Locate and identify every blood parasite.
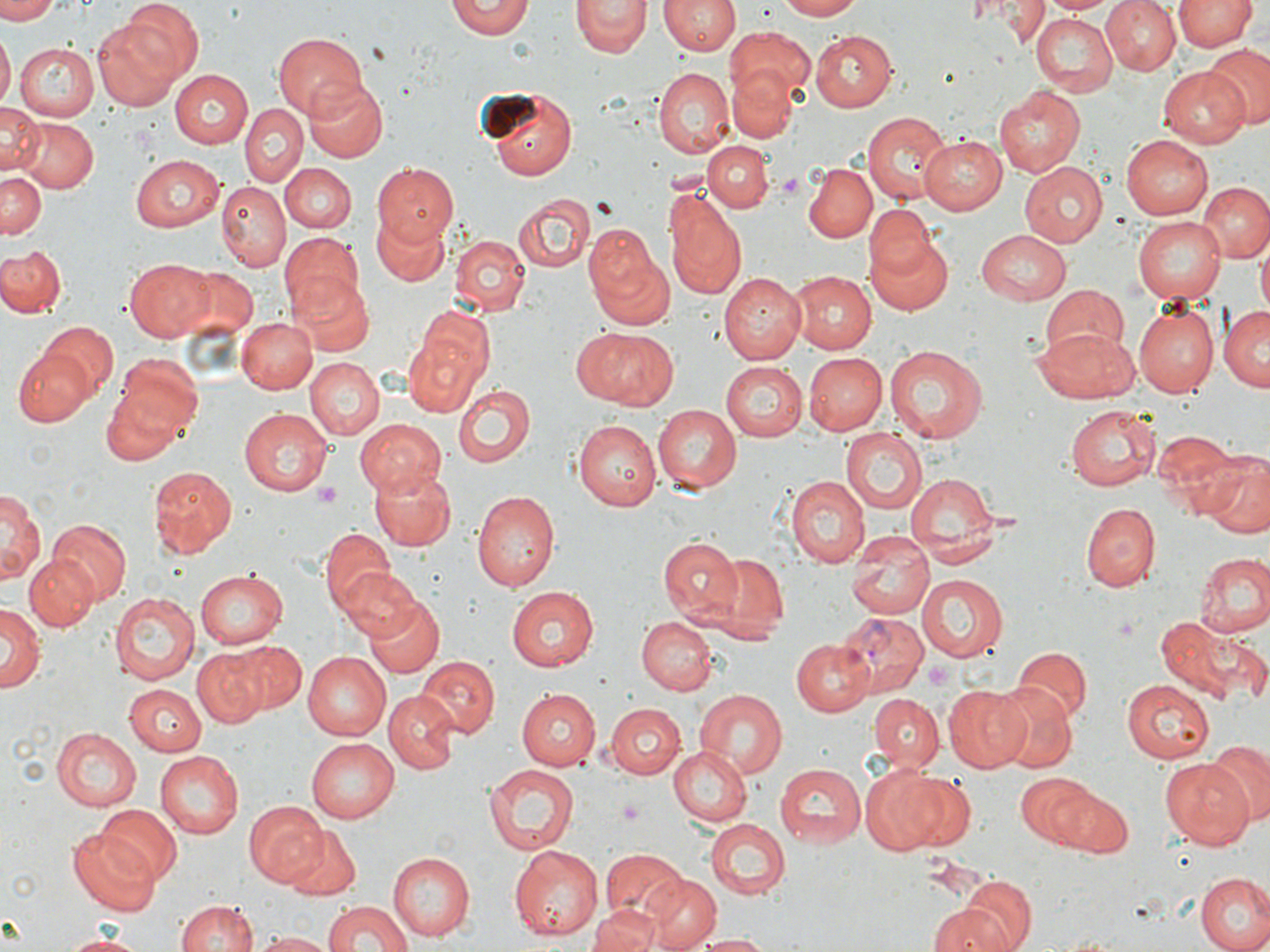
Approximate bounding boxes as named x1/y1/x2/y2 corners in pixels.
Plasmodium vivax-infected red blood cells: (x1=834, y1=614, x2=934, y2=701).
No Plasmodium falciparum, Plasmodium ovale, Plasmodium malariae, Babesia divergens, or Trypanosoma brucei observed.

slide_level_diagnosis: Plasmodium vivax
stain: May-Grünwald-Giemsa
image_size: 1270×952 pixels
platelet_locations: 'approximate bounding boxes as named x1/y1/x2/y2 corners in pixels: (x1=779, y1=172, x2=804, y2=199), (x1=314, y1=483, x2=343, y2=503), (x1=924, y1=659, x2=953, y2=687)'
magnification: 1000x
field_of_view: single
modality: optical microscopy
preparation: thin blood film
uninfected_red_blood_cell_locations: 'approximate bounding boxes as named x1/y1/x2/y2 corners in pixels: (x1=0, y1=0, x2=58, y2=23), (x1=118, y1=0, x2=204, y2=83), (x1=446, y1=0, x2=535, y2=40), (x1=572, y1=0, x2=649, y2=57), (x1=775, y1=0, x2=865, y2=20), (x1=958, y1=0, x2=1013, y2=23), (x1=1039, y1=0, x2=1113, y2=16), (x1=1100, y1=0, x2=1179, y2=75), (x1=1173, y1=0, x2=1254, y2=51), (x1=661, y1=1, x2=737, y2=57), (x1=987, y1=2, x2=1051, y2=43), (x1=1029, y1=12, x2=1116, y2=95), (x1=93, y1=19, x2=183, y2=112), (x1=724, y1=26, x2=816, y2=110), (x1=810, y1=29, x2=897, y2=112), (x1=273, y1=30, x2=365, y2=117), (x1=0, y1=33, x2=13, y2=111), (x1=13, y1=43, x2=97, y2=120), (x1=1202, y1=46, x2=1268, y2=132), (x1=727, y1=66, x2=799, y2=143), (x1=1157, y1=66, x2=1251, y2=147), (x1=170, y1=69, x2=253, y2=147), (x1=653, y1=69, x2=733, y2=158), (x1=301, y1=80, x2=388, y2=163), (x1=478, y1=84, x2=577, y2=180), (x1=994, y1=85, x2=1086, y2=176), (x1=0, y1=101, x2=43, y2=178), (x1=241, y1=105, x2=307, y2=187), (x1=862, y1=112, x2=951, y2=205), (x1=13, y1=117, x2=98, y2=194), (x1=919, y1=135, x2=1005, y2=214), (x1=1121, y1=136, x2=1213, y2=219), (x1=702, y1=140, x2=772, y2=212), (x1=131, y1=155, x2=225, y2=231), (x1=372, y1=162, x2=456, y2=244), (x1=803, y1=162, x2=874, y2=242), (x1=1020, y1=162, x2=1108, y2=247), (x1=282, y1=164, x2=355, y2=232), (x1=0, y1=167, x2=47, y2=238), (x1=1197, y1=180, x2=1270, y2=263), (x1=218, y1=182, x2=289, y2=269), (x1=514, y1=191, x2=596, y2=274), (x1=666, y1=195, x2=748, y2=302), (x1=866, y1=205, x2=937, y2=285), (x1=372, y1=213, x2=450, y2=289), (x1=1133, y1=216, x2=1226, y2=304), (x1=585, y1=221, x2=673, y2=320), (x1=976, y1=229, x2=1072, y2=302), (x1=867, y1=232, x2=955, y2=315), (x1=281, y1=233, x2=366, y2=321), (x1=450, y1=235, x2=529, y2=315), (x1=1257, y1=241, x2=1270, y2=318), (x1=1, y1=243, x2=65, y2=316), (x1=124, y1=258, x2=215, y2=342), (x1=171, y1=265, x2=259, y2=347), (x1=789, y1=271, x2=876, y2=353), (x1=719, y1=273, x2=808, y2=363), (x1=294, y1=278, x2=372, y2=355), (x1=1039, y1=288, x2=1131, y2=362), (x1=1132, y1=301, x2=1221, y2=398), (x1=405, y1=306, x2=496, y2=406), (x1=1220, y1=306, x2=1269, y2=390), (x1=236, y1=318, x2=318, y2=394), (x1=43, y1=320, x2=117, y2=396), (x1=577, y1=327, x2=677, y2=409), (x1=1033, y1=327, x2=1138, y2=405), (x1=885, y1=344, x2=990, y2=443), (x1=12, y1=348, x2=95, y2=427), (x1=804, y1=352, x2=887, y2=433), (x1=117, y1=353, x2=205, y2=436), (x1=305, y1=357, x2=383, y2=438), (x1=720, y1=361, x2=807, y2=441), (x1=102, y1=376, x2=197, y2=462), (x1=455, y1=386, x2=535, y2=468), (x1=652, y1=403, x2=743, y2=494), (x1=1066, y1=405, x2=1161, y2=491), (x1=241, y1=407, x2=337, y2=495), (x1=354, y1=419, x2=447, y2=496), (x1=575, y1=419, x2=660, y2=511), (x1=1152, y1=427, x2=1245, y2=519), (x1=840, y1=428, x2=929, y2=517), (x1=1200, y1=452, x2=1270, y2=539), (x1=367, y1=466, x2=456, y2=550), (x1=148, y1=467, x2=237, y2=557), (x1=903, y1=471, x2=1000, y2=558), (x1=787, y1=476, x2=868, y2=566), (x1=2, y1=490, x2=42, y2=587), (x1=472, y1=490, x2=560, y2=591), (x1=1080, y1=501, x2=1160, y2=592), (x1=48, y1=520, x2=130, y2=606), (x1=321, y1=527, x2=398, y2=615), (x1=660, y1=537, x2=745, y2=621), (x1=847, y1=541, x2=932, y2=621), (x1=699, y1=550, x2=788, y2=642), (x1=1195, y1=552, x2=1269, y2=639), (x1=23, y1=555, x2=97, y2=629), (x1=337, y1=567, x2=421, y2=645), (x1=195, y1=569, x2=286, y2=650), (x1=917, y1=575, x2=1007, y2=661), (x1=506, y1=586, x2=599, y2=672), (x1=109, y1=592, x2=200, y2=683), (x1=364, y1=596, x2=445, y2=679), (x1=1, y1=603, x2=43, y2=694), (x1=1155, y1=611, x2=1266, y2=705), (x1=638, y1=617, x2=716, y2=695), (x1=790, y1=638, x2=875, y2=716), (x1=234, y1=641, x2=307, y2=714), (x1=1013, y1=648, x2=1091, y2=723), (x1=192, y1=649, x2=268, y2=726), (x1=301, y1=652, x2=390, y2=740), (x1=417, y1=657, x2=499, y2=738), (x1=1123, y1=679, x2=1217, y2=761), (x1=995, y1=681, x2=1076, y2=772), (x1=123, y1=685, x2=207, y2=755), (x1=945, y1=685, x2=1034, y2=772), (x1=516, y1=688, x2=600, y2=770), (x1=693, y1=689, x2=787, y2=779), (x1=384, y1=692, x2=456, y2=774), (x1=869, y1=693, x2=944, y2=771), (x1=604, y1=703, x2=685, y2=779), (x1=51, y1=727, x2=141, y2=810), (x1=307, y1=738, x2=397, y2=824), (x1=1208, y1=739, x2=1270, y2=823), (x1=669, y1=745, x2=750, y2=826), (x1=155, y1=750, x2=244, y2=838), (x1=1161, y1=757, x2=1256, y2=847), (x1=775, y1=762, x2=865, y2=847), (x1=484, y1=764, x2=579, y2=855), (x1=858, y1=766, x2=952, y2=854), (x1=1016, y1=771, x2=1094, y2=848), (x1=902, y1=773, x2=975, y2=853), (x1=1056, y1=785, x2=1134, y2=857), (x1=244, y1=801, x2=329, y2=891), (x1=94, y1=806, x2=179, y2=885), (x1=705, y1=819, x2=790, y2=899), (x1=281, y1=824, x2=363, y2=900), (x1=69, y1=832, x2=163, y2=916), (x1=509, y1=844, x2=604, y2=941), (x1=600, y1=848, x2=686, y2=925), (x1=391, y1=850, x2=476, y2=940), (x1=1195, y1=872, x2=1270, y2=952), (x1=645, y1=876, x2=720, y2=951), (x1=960, y1=877, x2=1034, y2=952), (x1=175, y1=898, x2=255, y2=952), (x1=323, y1=901, x2=414, y2=952), (x1=928, y1=902, x2=1019, y2=952), (x1=590, y1=904, x2=664, y2=952), (x1=258, y1=931, x2=332, y2=951), (x1=54, y1=932, x2=156, y2=951), (x1=689, y1=932, x2=771, y2=952)'